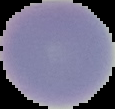
Segmented cell region on a black background. Image is 115×109 pixels. Result: no Plasmodium parasites seen. From a thin blood film.